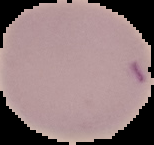

Result: negative for malaria parasites. Image is 154×145 pixels. The area outside the segmented cell region is set to black. From a thin blood smear.